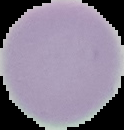
Summary:
  - Result: negative for Plasmodium parasites
  - Image type: cell region segmented out of the field of view; surrounding area masked to black
  - Image size: 124×130 pixels
  - Preparation: thin blood smear